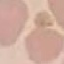

Summary:
  - Malaria status: uninfected
  - Stain: Giemsa
  - Preparation: thin blood film
  - Image type: cell patch, automatically extracted from a larger field of view and resized to 64 × 64 pixels
  - Capture: smartphone camera at the microscope eyepiece